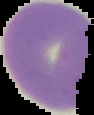
Summary:
  - Malaria status: uninfected
  - Preparation: thin blood smear
  - Image type: segmented cell region with the area outside set to black
  - Image size: 94×115 pixels